Classify this cell by malaria status.
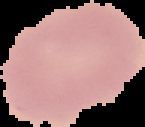

It is uninfected.

Cell region segmented out of the field of view; the surrounding area is masked to black. Image is 145×127 pixels. From a thin blood smear.